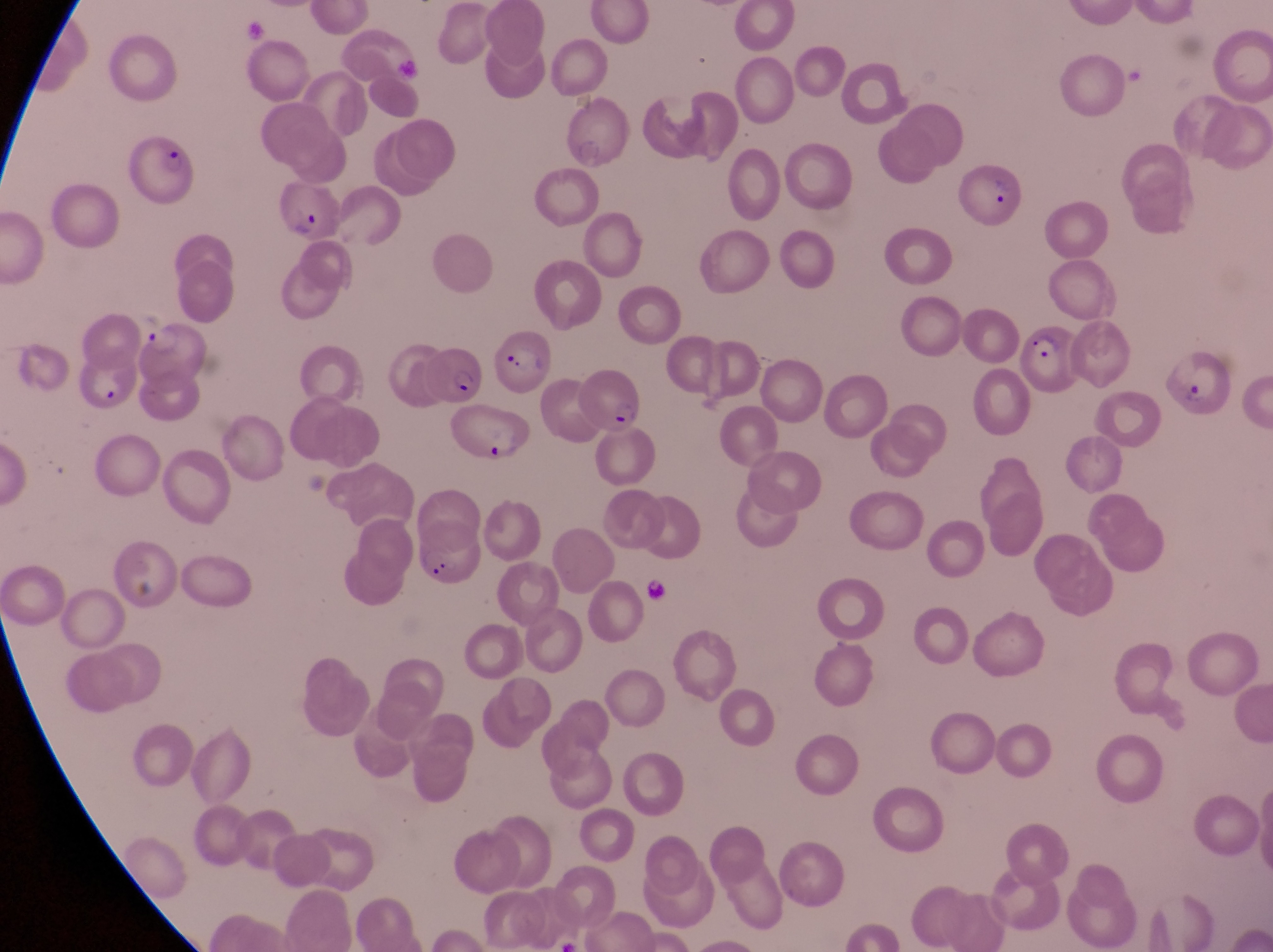 Approximate bounding boxes as left top right bottom in pixels. Parasitised red blood cell locations: 118 137 198 204; 953 169 1022 231; 269 177 338 242; 1013 325 1093 399; 139 327 213 392; 497 337 557 400; 1171 342 1228 417; 426 348 489 410; 70 354 139 419; 577 374 642 437; 440 412 528 469; 407 514 481 588. At a magnification of 1000x. Image is 1273×952 pixels. Captured by a smartphone held over the eyepiece of an Olympus CX-23 microscope. Collected in Uganda. One field of view. Thin blood film.